Classify this cell by malaria status.
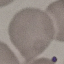
Uninfected.

Summary:
  - Preparation: thin smear
  - Image type: automatically extracted cell patch, resized to 64 × 64 pixels
  - Stain: Giemsa
  - Capture: smartphone through the microscope eyepiece